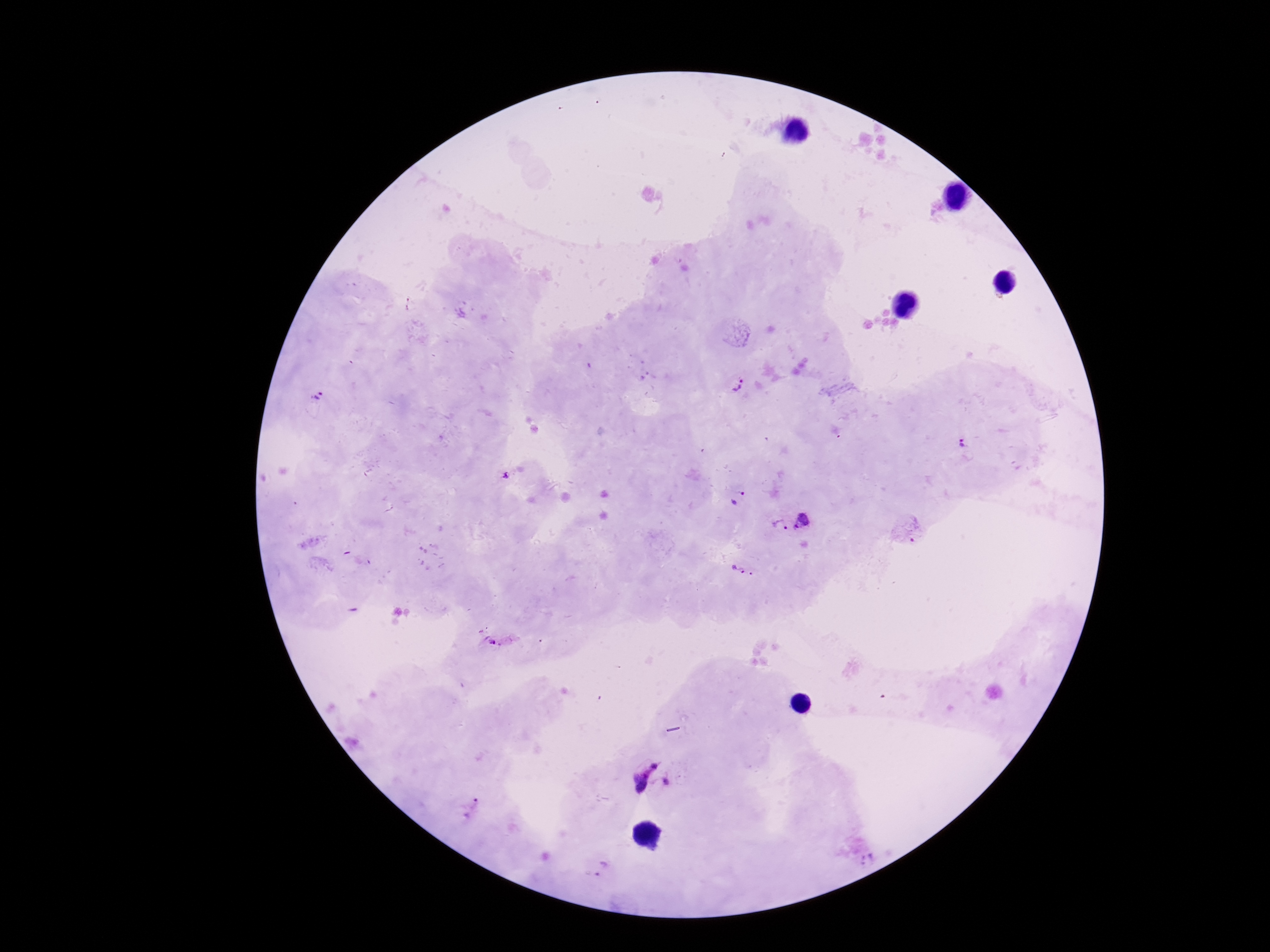
Approximate centers as [x, y] in pixels.
Summary:
  - Plasmodium parasite locations: [737, 386], [318, 396], [964, 443], [506, 477], [735, 498], [805, 521], [780, 526], [907, 529], [743, 570], [492, 641], [637, 768], [668, 784], [474, 808], [867, 860], [601, 867]
  - Preparation: thick blood film
  - Magnification: 100x
  - Image size: 1270×952 pixels
  - Capture: smartphone camera through the microscope eyepiece
  - Patient malaria status: infected
  - Stain: Giemsa
  - Field of view: single